Identify the blood parasite species.
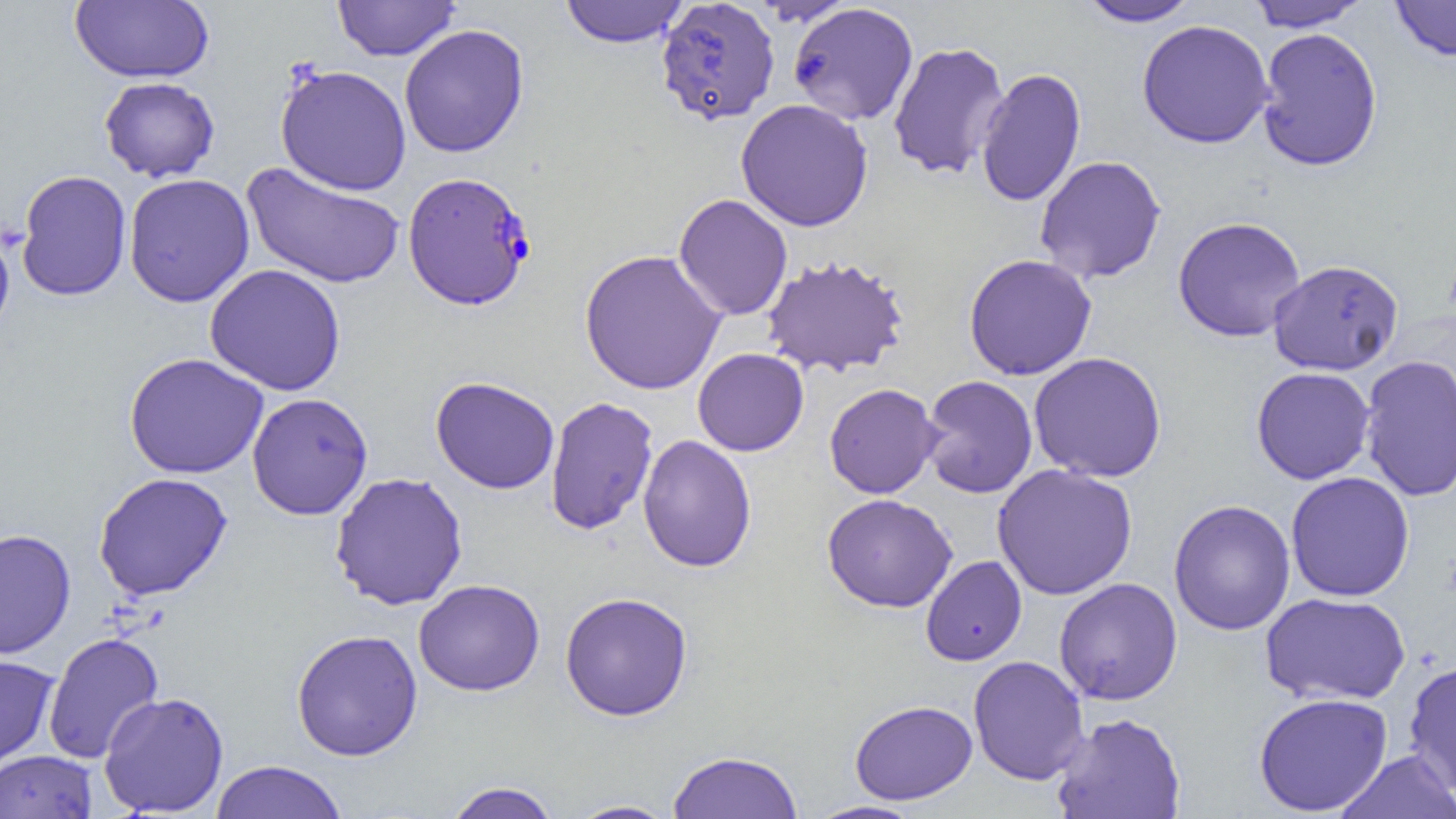

Plasmodium falciparum.

uninfected red blood cell locations = approximate bounding boxes as named x1/y1/x2/y2 corners in pixels: (x1=70, y1=0, x2=214, y2=84), (x1=333, y1=0, x2=460, y2=61), (x1=1077, y1=0, x2=1203, y2=27), (x1=1389, y1=0, x2=1456, y2=61), (x1=559, y1=1, x2=689, y2=47), (x1=655, y1=1, x2=780, y2=126), (x1=1244, y1=1, x2=1372, y2=31), (x1=787, y1=2, x2=919, y2=126), (x1=1137, y1=19, x2=1274, y2=149), (x1=399, y1=24, x2=529, y2=158), (x1=1255, y1=27, x2=1383, y2=172), (x1=887, y1=42, x2=1010, y2=180), (x1=275, y1=64, x2=412, y2=196), (x1=975, y1=67, x2=1086, y2=208), (x1=99, y1=76, x2=220, y2=182), (x1=735, y1=99, x2=874, y2=232), (x1=1034, y1=155, x2=1166, y2=284), (x1=242, y1=163, x2=406, y2=290), (x1=15, y1=170, x2=132, y2=301), (x1=123, y1=173, x2=255, y2=307), (x1=673, y1=194, x2=793, y2=320), (x1=1172, y1=216, x2=1306, y2=342), (x1=0, y1=218, x2=15, y2=345), (x1=579, y1=249, x2=728, y2=395), (x1=963, y1=253, x2=1098, y2=381), (x1=762, y1=254, x2=910, y2=378), (x1=1268, y1=259, x2=1404, y2=375), (x1=205, y1=263, x2=346, y2=395), (x1=693, y1=348, x2=809, y2=456), (x1=1028, y1=351, x2=1167, y2=483), (x1=124, y1=352, x2=269, y2=479), (x1=1359, y1=354, x2=1456, y2=502), (x1=1251, y1=367, x2=1375, y2=485), (x1=920, y1=375, x2=1037, y2=498), (x1=430, y1=376, x2=560, y2=494), (x1=824, y1=383, x2=942, y2=499), (x1=247, y1=392, x2=373, y2=520), (x1=544, y1=396, x2=659, y2=536), (x1=637, y1=434, x2=757, y2=573), (x1=992, y1=463, x2=1138, y2=600), (x1=1285, y1=471, x2=1415, y2=602), (x1=93, y1=472, x2=233, y2=600), (x1=329, y1=472, x2=468, y2=611), (x1=821, y1=493, x2=958, y2=613), (x1=1168, y1=499, x2=1296, y2=636), (x1=0, y1=529, x2=76, y2=660), (x1=920, y1=555, x2=1027, y2=666), (x1=1054, y1=577, x2=1182, y2=705), (x1=413, y1=579, x2=545, y2=696), (x1=560, y1=591, x2=693, y2=721), (x1=1260, y1=592, x2=1411, y2=705), (x1=291, y1=629, x2=423, y2=761), (x1=43, y1=632, x2=164, y2=764), (x1=0, y1=655, x2=59, y2=770), (x1=968, y1=655, x2=1089, y2=785), (x1=1403, y1=659, x2=1456, y2=797), (x1=98, y1=692, x2=229, y2=817), (x1=1253, y1=692, x2=1393, y2=816), (x1=850, y1=700, x2=977, y2=805), (x1=1051, y1=711, x2=1186, y2=819), (x1=0, y1=750, x2=97, y2=819), (x1=667, y1=750, x2=803, y2=818), (x1=1335, y1=750, x2=1456, y2=819), (x1=209, y1=759, x2=348, y2=818), (x1=442, y1=781, x2=563, y2=819), (x1=566, y1=800, x2=679, y2=818), (x1=805, y1=800, x2=924, y2=819)
Plasmodium falciparum-infected red blood cell locations = approximate bounding boxes as named x1/y1/x2/y2 corners in pixels: (x1=402, y1=171, x2=536, y2=310)
magnification = 1000x
field of view = one of a larger specimen
preparation = thin blood smear
image size = 1456×819 pixels
modality = optical microscopy